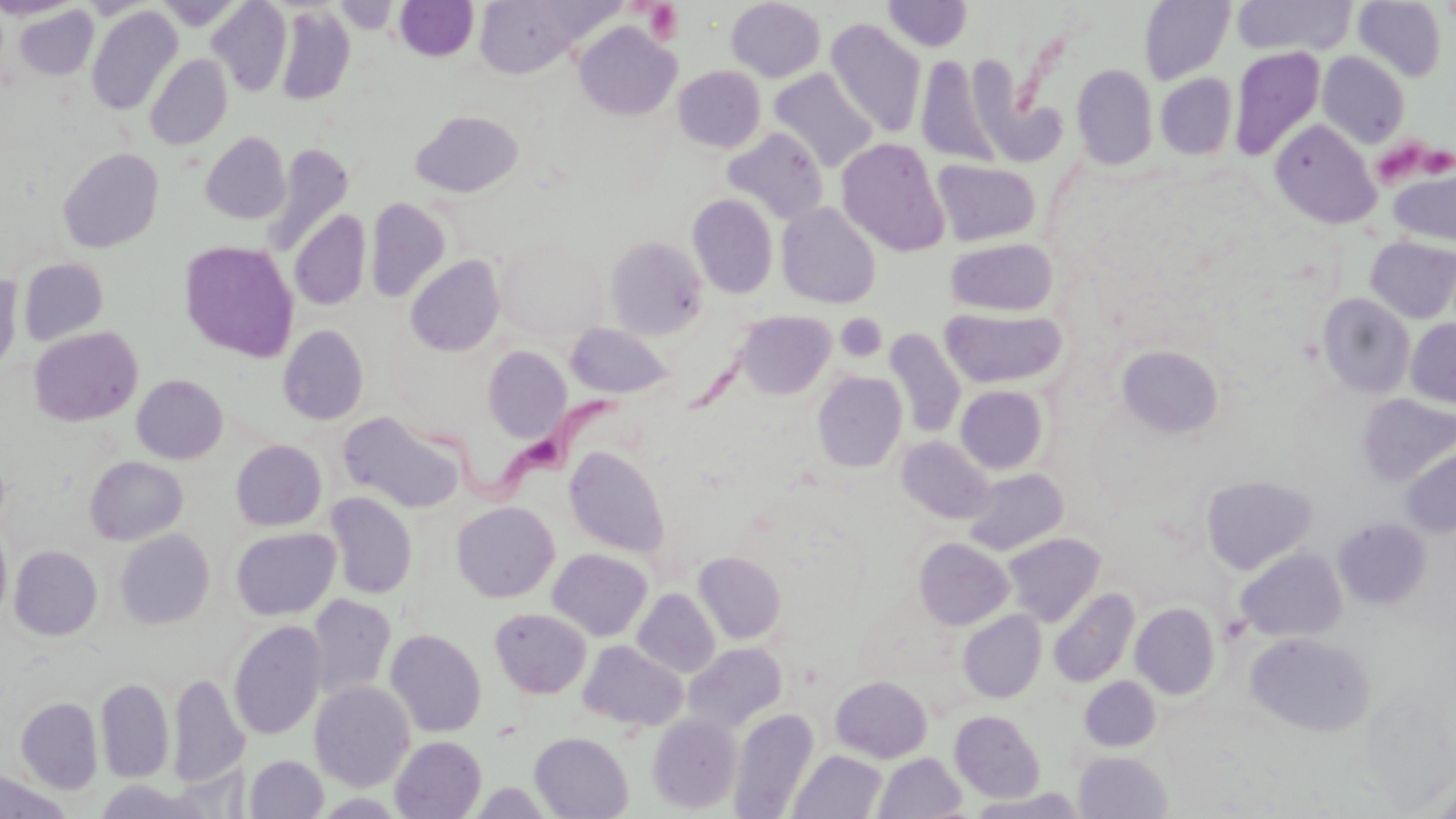
slide_level_diagnosis: Trypanosoma brucei
uninfected_red_blood_cell_locations: 'approximate bounding boxes as (x1, y1, x2, y2) in pixels: (0, 0, 82, 19), (474, 0, 581, 78), (726, 0, 826, 82), (883, 0, 973, 52), (1232, 0, 1355, 57), (1354, 0, 1446, 82), (207, 1, 293, 97), (394, 1, 479, 62), (1139, 1, 1235, 84), (151, 2, 247, 30), (337, 2, 397, 33), (274, 4, 355, 105), (13, 5, 99, 80), (86, 6, 183, 116), (825, 19, 928, 137), (574, 21, 682, 121), (1230, 46, 1326, 161), (1318, 52, 1410, 148), (145, 54, 232, 150), (915, 54, 1002, 166), (1073, 64, 1158, 169), (673, 65, 766, 152), (769, 68, 879, 173), (969, 68, 1066, 167), (1156, 73, 1237, 159), (411, 110, 523, 197), (1270, 119, 1381, 229), (722, 127, 829, 225), (201, 131, 290, 225), (836, 137, 950, 256), (263, 143, 354, 258), (58, 148, 163, 253), (932, 158, 1042, 246), (1388, 167, 1456, 247), (688, 194, 778, 299), (365, 197, 451, 302), (777, 203, 880, 309), (290, 209, 371, 311), (604, 235, 708, 339), (494, 237, 605, 339), (1366, 237, 1456, 323), (946, 238, 1058, 317), (179, 240, 299, 363), (405, 255, 505, 356), (19, 258, 108, 345), (0, 272, 22, 376), (1318, 294, 1415, 398), (940, 307, 1066, 389), (736, 310, 835, 398), (1406, 319, 1456, 407), (565, 323, 675, 399), (278, 325, 369, 424), (28, 326, 142, 426), (884, 328, 966, 439), (1116, 345, 1224, 438), (482, 346, 571, 443), (812, 372, 907, 472), (131, 374, 227, 464), (955, 385, 1048, 474), (1358, 394, 1456, 485), (338, 411, 465, 513), (897, 436, 994, 523), (231, 439, 326, 531), (565, 445, 669, 557), (1401, 445, 1456, 538), (85, 456, 187, 545), (964, 468, 1069, 555), (1201, 474, 1317, 575), (325, 492, 417, 598), (452, 501, 559, 602), (1334, 518, 1431, 608), (0, 525, 11, 623), (230, 527, 340, 620), (116, 529, 214, 629), (1003, 533, 1105, 626), (914, 538, 1014, 630), (9, 546, 102, 640), (1236, 547, 1347, 642), (548, 549, 652, 641), (693, 552, 786, 644), (1048, 587, 1139, 687), (633, 588, 720, 677), (308, 593, 396, 700), (1131, 603, 1219, 699), (490, 608, 591, 698), (958, 610, 1046, 703), (228, 620, 327, 740), (385, 629, 487, 737), (1245, 632, 1375, 736), (579, 641, 688, 732), (684, 642, 787, 732), (168, 673, 248, 788), (830, 676, 932, 763), (1082, 676, 1160, 750), (96, 679, 174, 783), (310, 681, 415, 791), (17, 697, 103, 793), (729, 709, 818, 818), (950, 710, 1045, 802), (647, 713, 742, 813), (530, 732, 633, 818), (391, 736, 486, 818), (789, 750, 887, 819), (1074, 751, 1172, 818), (874, 752, 967, 818), (246, 755, 329, 818), (0, 769, 71, 818), (94, 780, 208, 819), (315, 793, 407, 817)'
modality: optical microscopy
magnification: 1000x
stain: May-Grünwald-Giemsa
trypanosoma_brucei_locations: 'approximate bounding boxes as (x1, y1, x2, y2) in pixels: (408, 388, 635, 506)'
preparation: thin blood film
field_of_view: one of a larger specimen
platelet_locations: 'approximate bounding boxes as (x1, y1, x2, y2) in pixels: (644, 2, 684, 43), (1375, 135, 1424, 183), (1422, 147, 1456, 174), (837, 313, 886, 361)'
image_size: 1456×819 pixels